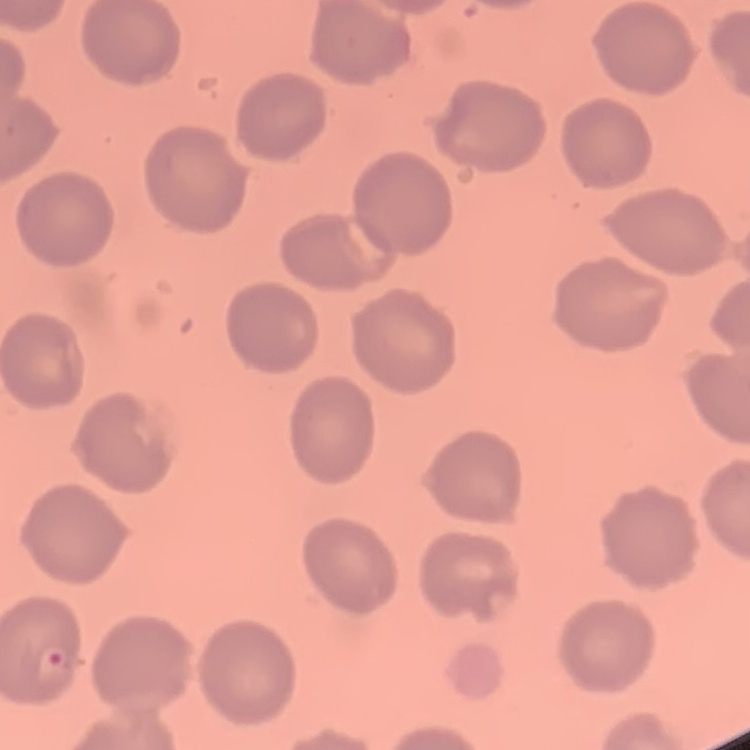

Summary:
  - Erythrocyte morphology: no rouleaux formation
  - Image type: square crop of a larger photomicrograph
  - Stain: Field's or Giemsa
  - Preparation: thin blood film